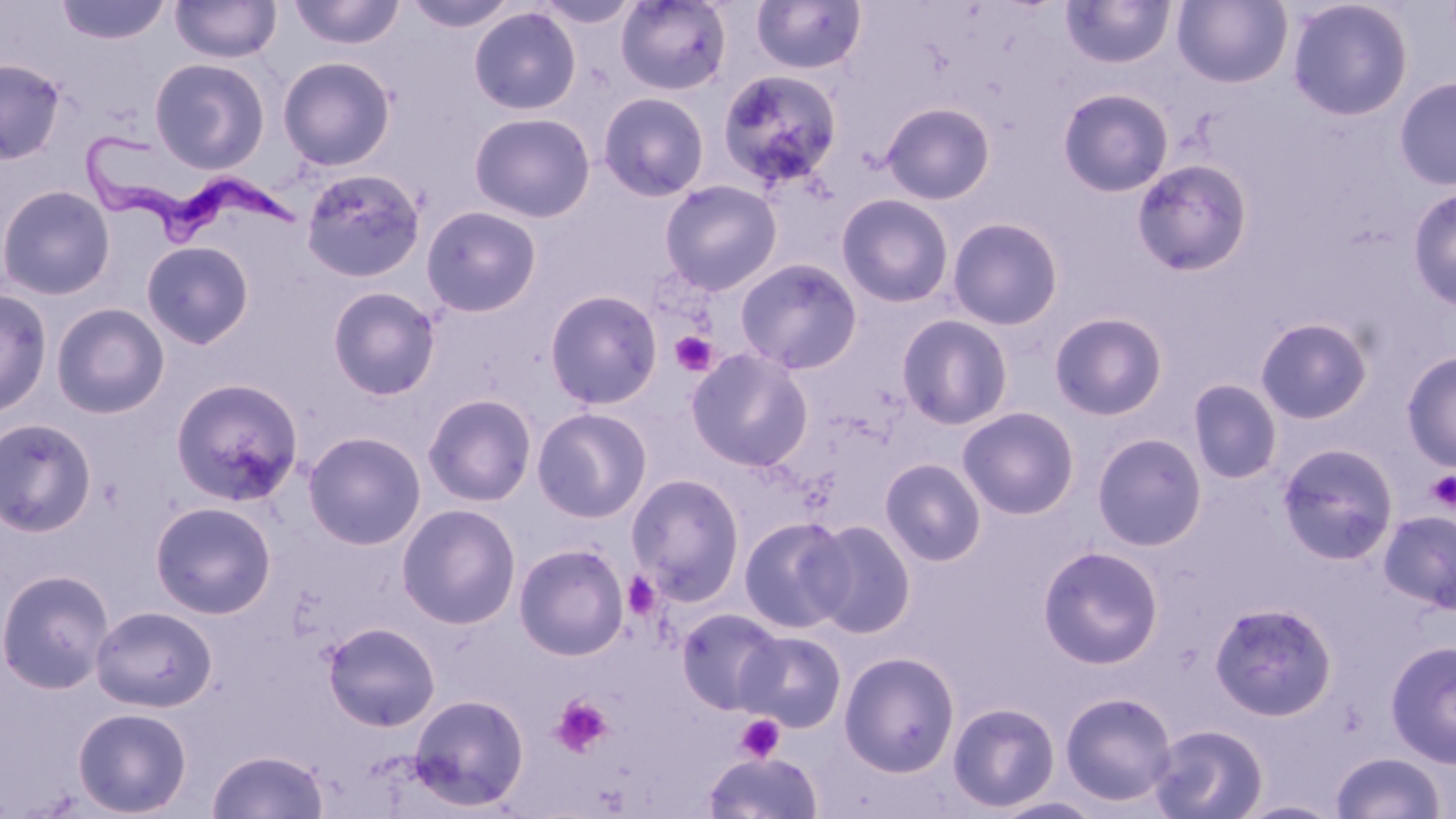 Approximate bounding boxes as named x1/y1/x2/y2 corners in pixels. Uninfected red blood cell locations: (x1=289, y1=0, x2=405, y2=50), (x1=534, y1=0, x2=641, y2=29), (x1=616, y1=0, x2=732, y2=96), (x1=750, y1=0, x2=868, y2=76), (x1=1172, y1=0, x2=1293, y2=88), (x1=1287, y1=0, x2=1413, y2=121), (x1=55, y1=1, x2=171, y2=45), (x1=170, y1=1, x2=282, y2=63), (x1=404, y1=1, x2=518, y2=33), (x1=1059, y1=1, x2=1176, y2=70), (x1=468, y1=6, x2=582, y2=115), (x1=278, y1=55, x2=396, y2=171), (x1=149, y1=56, x2=270, y2=174), (x1=0, y1=58, x2=65, y2=164), (x1=716, y1=69, x2=842, y2=189), (x1=1394, y1=77, x2=1456, y2=191), (x1=1058, y1=88, x2=1174, y2=197), (x1=598, y1=92, x2=710, y2=201), (x1=881, y1=101, x2=995, y2=205), (x1=468, y1=111, x2=595, y2=222), (x1=1132, y1=159, x2=1253, y2=276), (x1=300, y1=167, x2=426, y2=283), (x1=659, y1=179, x2=783, y2=295), (x1=0, y1=184, x2=116, y2=300), (x1=1407, y1=188, x2=1456, y2=310), (x1=836, y1=193, x2=955, y2=308), (x1=420, y1=206, x2=542, y2=317), (x1=947, y1=216, x2=1065, y2=330), (x1=141, y1=241, x2=254, y2=349), (x1=735, y1=258, x2=863, y2=374), (x1=327, y1=286, x2=441, y2=400), (x1=0, y1=288, x2=52, y2=417), (x1=544, y1=289, x2=664, y2=409), (x1=50, y1=303, x2=170, y2=419), (x1=1049, y1=312, x2=1168, y2=421), (x1=896, y1=313, x2=1013, y2=430), (x1=1255, y1=316, x2=1373, y2=424), (x1=686, y1=347, x2=813, y2=471), (x1=1401, y1=351, x2=1456, y2=471), (x1=170, y1=377, x2=303, y2=505), (x1=1187, y1=379, x2=1283, y2=485), (x1=413, y1=392, x2=530, y2=622), (x1=422, y1=393, x2=537, y2=507), (x1=532, y1=406, x2=653, y2=523), (x1=957, y1=406, x2=1080, y2=519), (x1=0, y1=417, x2=97, y2=537), (x1=303, y1=431, x2=427, y2=550), (x1=1092, y1=433, x2=1208, y2=551), (x1=1277, y1=442, x2=1399, y2=565), (x1=879, y1=458, x2=986, y2=566), (x1=625, y1=473, x2=746, y2=603), (x1=149, y1=500, x2=277, y2=619), (x1=396, y1=503, x2=521, y2=629), (x1=1378, y1=510, x2=1456, y2=613), (x1=738, y1=516, x2=852, y2=632), (x1=807, y1=519, x2=916, y2=638), (x1=513, y1=543, x2=629, y2=660), (x1=1038, y1=545, x2=1164, y2=669), (x1=0, y1=568, x2=115, y2=694), (x1=1209, y1=601, x2=1338, y2=721), (x1=90, y1=605, x2=217, y2=712), (x1=674, y1=607, x2=786, y2=712), (x1=322, y1=621, x2=441, y2=731), (x1=737, y1=630, x2=847, y2=732), (x1=1385, y1=640, x2=1456, y2=767), (x1=839, y1=650, x2=960, y2=777), (x1=1059, y1=691, x2=1178, y2=807), (x1=407, y1=693, x2=529, y2=812), (x1=947, y1=701, x2=1060, y2=812), (x1=72, y1=707, x2=193, y2=817), (x1=1149, y1=723, x2=1268, y2=819), (x1=207, y1=749, x2=328, y2=819), (x1=1330, y1=751, x2=1445, y2=818), (x1=703, y1=752, x2=823, y2=819), (x1=987, y1=795, x2=1107, y2=819). Platelet locations: (x1=670, y1=331, x2=718, y2=376), (x1=1426, y1=469, x2=1456, y2=511), (x1=621, y1=572, x2=662, y2=620), (x1=550, y1=694, x2=614, y2=758), (x1=735, y1=714, x2=784, y2=763). Trypanosoma brucei locations: (x1=72, y1=122, x2=311, y2=249). Slide-level diagnosis: Trypanosoma brucei. Thin blood smear. One field of a larger specimen. Image is 1456×819 pixels. 1000x magnification. Optical microscopy. May-Grünwald-Giemsa-stained preparation.